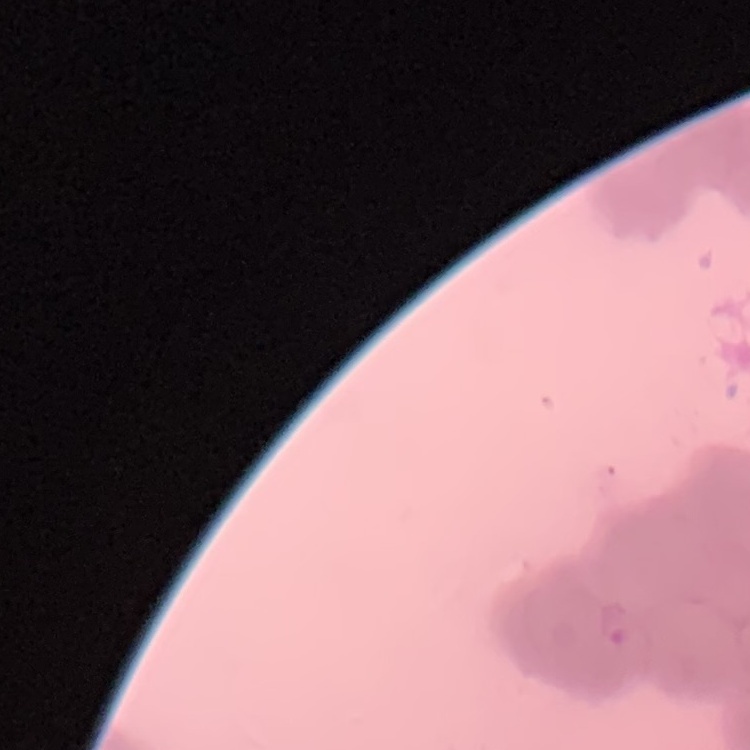

The erythrocytes exhibit rouleaux formation. Field's or Giemsa stain. Thin blood film. Square crop of a larger photomicrograph.